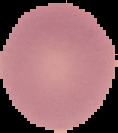

image size = 118×133 pixels
image type = segmented cell region with the area outside set to black
result = no Plasmodium parasites seen
preparation = thin blood film